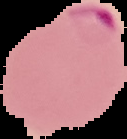
Summary:
  - Image size: 127×139 pixels
  - Malaria status: parasitized
  - Image type: cell region segmented out of the field of view; surrounding area masked to black
  - Preparation: thin blood film